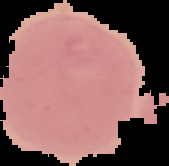

Summary:
  - Preparation: thin blood film
  - Image size: 169×166 pixels
  - Result: no malaria parasites seen
  - Image type: cell region segmented out of the field of view; surrounding area masked to black